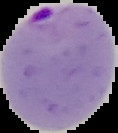
malaria status = parasitized
image type = segmented cell region on a black background
preparation = thin blood smear
image size = 118×133 pixels